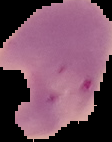

Summary:
  - Result: malaria parasites identified
  - Image type: segmented cell region with the area outside set to black
  - Image size: 112×142 pixels
  - Preparation: thin blood film